Report the malaria status of this cell.
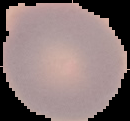

Uninfected.

{
  "image_size": "130×121 pixels",
  "preparation": "thin blood film",
  "image_type": "segmented cell region on a black background"
}